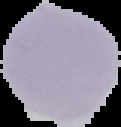
image type = segmented cell region on a black background
image size = 121×127 pixels
malaria status = uninfected
preparation = thin blood smear